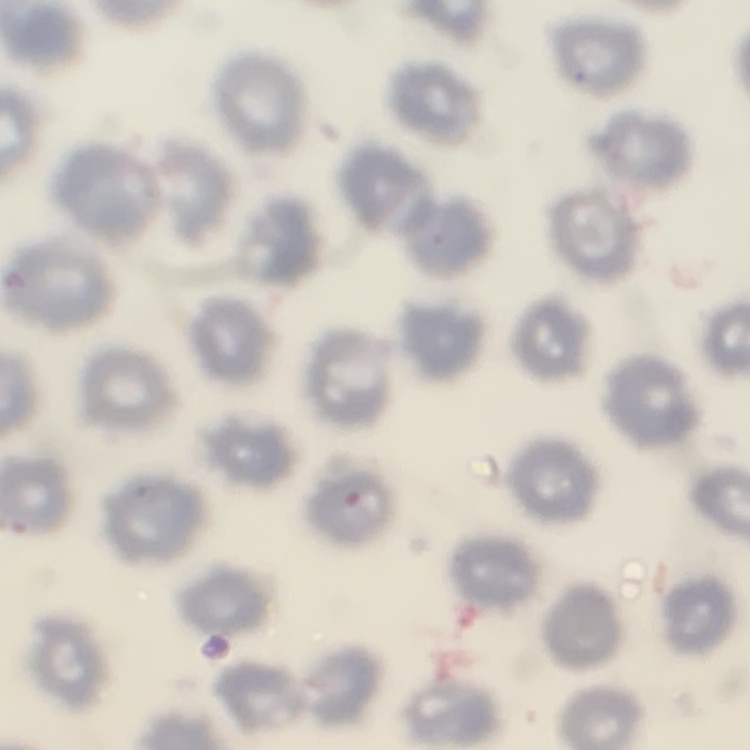

erythrocyte_morphology: no rouleaux formation
image_type: square crop of a larger photomicrograph
preparation: thin blood smear
stain: Field's or Giemsa